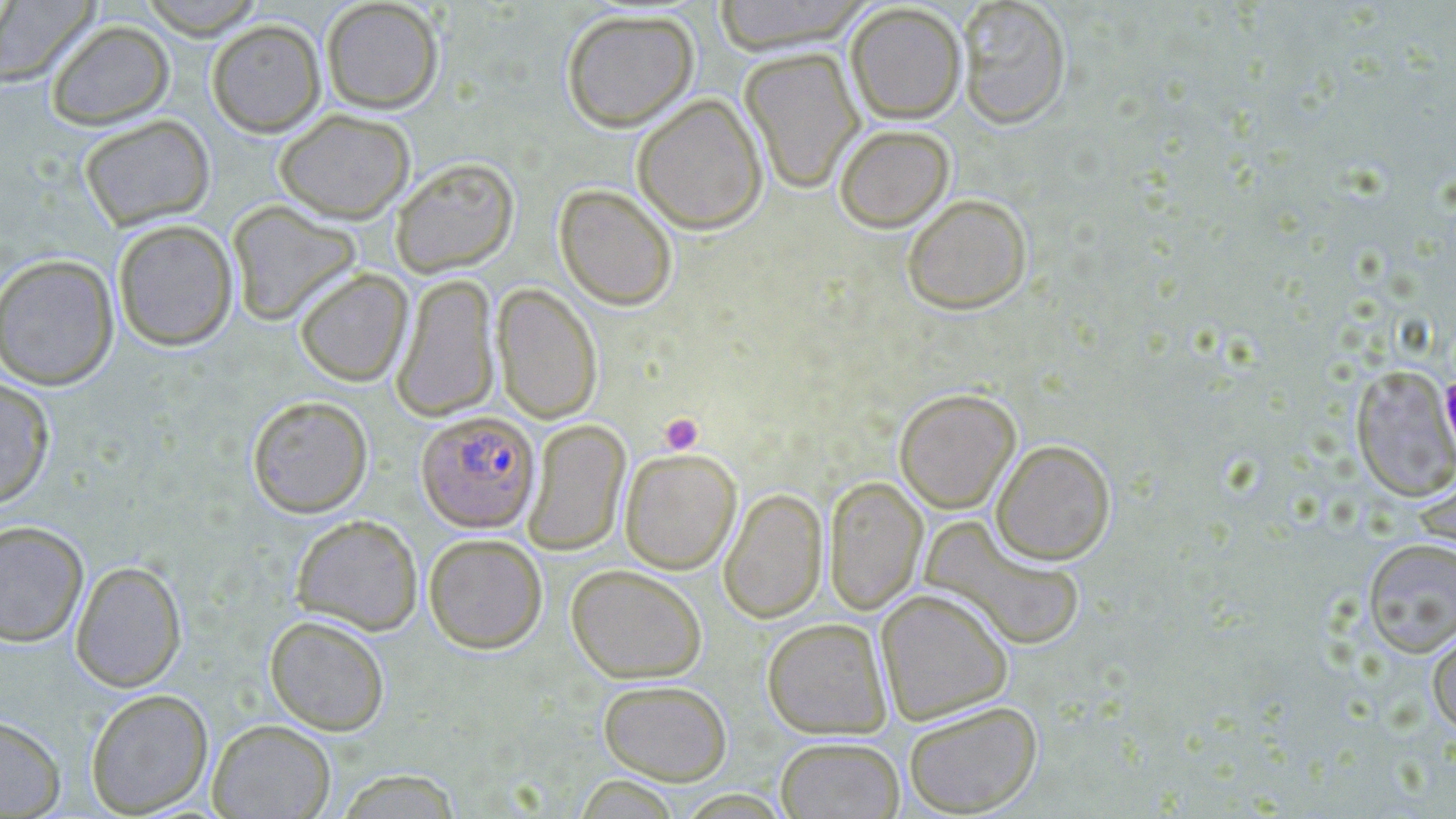
slide-level diagnosis = Plasmodium falciparum
stain = May-Grünwald-Giemsa
Plasmodium falciparum-infected red blood cell locations = approximate bounding boxes as (x1,y1)-(x2,y2) corner pairs in pixels: (416,410)-(540,533)
modality = light microscopy
image size = 1456×819 pixels
preparation = thin blood smear
field of view = single
uninfected red blood cell locations = approximate bounding boxes as (x1,y1)-(x2,y2) corner pairs in pixels: (0,0)-(99,86), (136,0)-(269,38), (320,0)-(444,114), (711,0)-(873,54), (955,0)-(1072,130), (845,3)-(967,124), (561,8)-(699,132), (45,19)-(175,130), (206,19)-(326,137), (740,47)-(864,193), (632,93)-(768,235), (274,108)-(416,223), (78,114)-(215,231), (834,124)-(955,232), (390,157)-(520,277), (554,183)-(678,311), (901,193)-(1033,315), (226,200)-(362,327), (112,218)-(238,351), (0,254)-(119,391), (294,267)-(413,387), (391,273)-(500,422), (492,283)-(604,425), (1351,366)-(1456,503), (0,376)-(56,508), (893,387)-(1022,513), (246,394)-(373,518), (523,419)-(631,556), (991,439)-(1116,565), (620,449)-(741,575), (1412,458)-(1456,565), (824,476)-(928,615), (719,487)-(828,624), (290,514)-(424,636), (920,517)-(1087,653), (0,520)-(89,648), (424,533)-(548,653), (1362,538)-(1456,658), (70,559)-(187,692), (566,564)-(707,683), (875,588)-(1014,725), (264,614)-(391,736), (762,617)-(892,739), (1427,623)-(1456,736), (598,678)-(733,785), (85,688)-(213,817), (902,700)-(1042,816), (0,714)-(66,817), (207,718)-(336,819), (775,736)-(905,819), (333,769)-(465,818), (572,776)-(685,818)
platelet locations = approximate bounding boxes as (x1,y1)-(x2,y2) corner pairs in pixels: (658,412)-(704,456)
magnification = 1000x